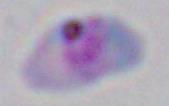 Toxoplasma gondii is shown. Photomicrograph. 1000x magnification.